Locate every blood parasite and identify its species.
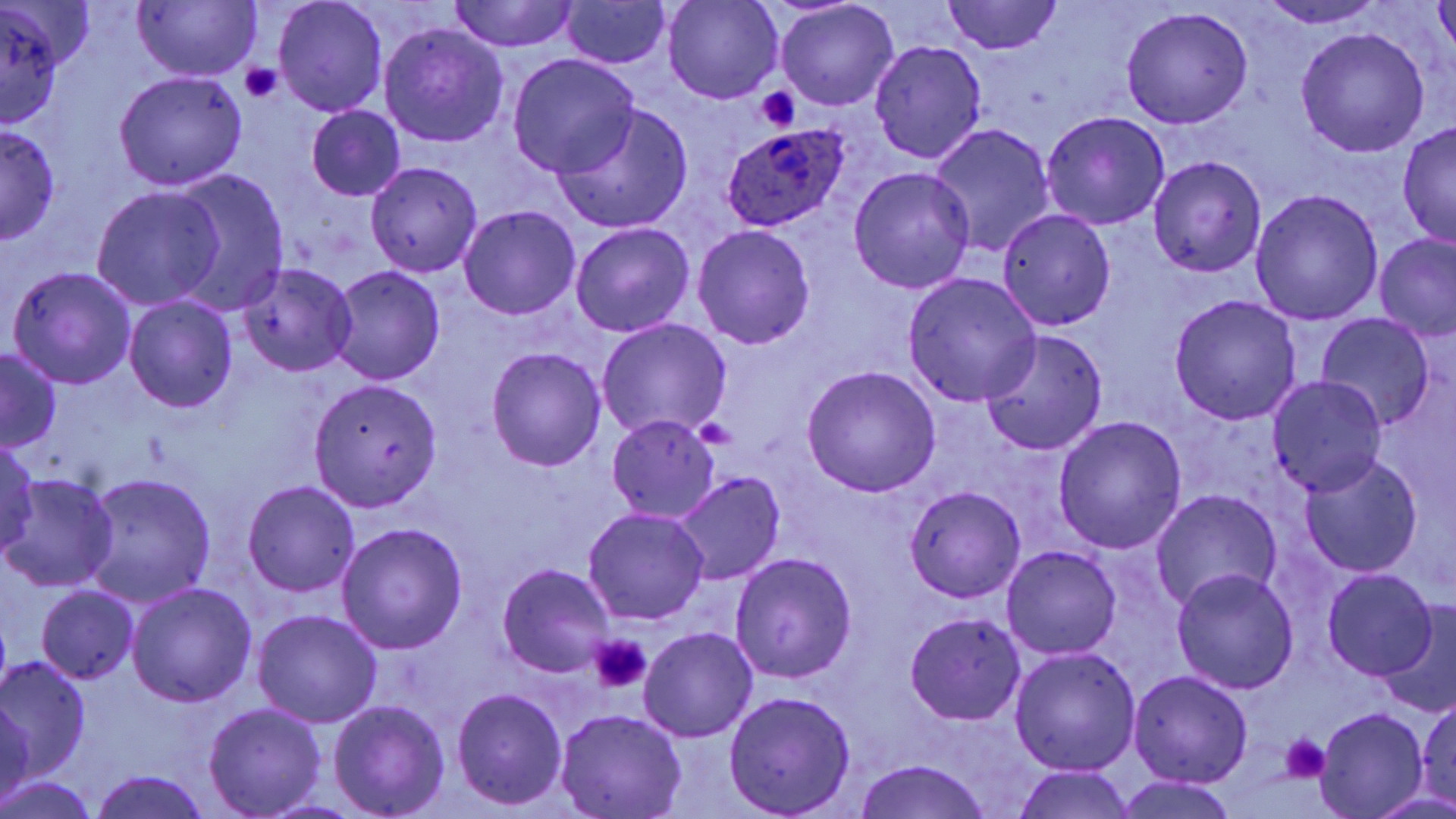

Approximate bounding boxes as (x1, y1, x2, y2) in pixels.
Plasmodium ovale-infected red blood cells: (720, 125, 847, 231).
No Plasmodium falciparum, Plasmodium malariae, Plasmodium vivax, Babesia divergens, or Trypanosoma brucei observed.

Uninfected red blood cell locations: (662, 0, 783, 104), (3, 1, 97, 73), (272, 1, 388, 116), (449, 1, 580, 53), (558, 1, 674, 70), (941, 1, 1064, 56), (1258, 1, 1389, 28), (775, 2, 900, 109), (1432, 2, 1456, 60), (1, 3, 66, 127), (131, 3, 260, 81), (1121, 7, 1254, 129), (380, 23, 508, 148), (1295, 27, 1429, 156), (869, 41, 988, 164), (508, 54, 639, 178), (114, 70, 247, 191), (553, 103, 693, 235), (306, 106, 405, 201), (1041, 111, 1171, 230), (1, 122, 60, 243), (928, 123, 1057, 256), (1397, 123, 1456, 248), (1148, 156, 1266, 278), (366, 161, 482, 277), (849, 167, 976, 293), (172, 170, 288, 308), (91, 187, 221, 310), (1250, 188, 1384, 326), (460, 205, 581, 318), (997, 209, 1116, 330), (570, 221, 696, 337), (692, 225, 816, 350), (1375, 235, 1456, 342), (238, 262, 359, 377), (8, 266, 137, 390), (330, 266, 445, 386), (903, 273, 1041, 407), (125, 295, 237, 414), (1170, 295, 1302, 426), (1315, 314, 1436, 432), (597, 318, 731, 442), (981, 328, 1107, 456), (486, 345, 607, 470), (1, 348, 63, 454), (802, 366, 941, 498), (1267, 376, 1389, 498), (308, 377, 443, 510), (606, 415, 719, 522), (1053, 416, 1187, 553), (1, 434, 42, 557), (1299, 454, 1423, 579), (669, 471, 786, 584), (3, 472, 119, 593), (82, 473, 216, 607), (242, 481, 360, 598), (904, 486, 1026, 603), (1151, 490, 1282, 615), (582, 506, 710, 626), (338, 523, 467, 653), (1002, 545, 1120, 659), (730, 553, 857, 682), (497, 563, 615, 677), (1172, 568, 1299, 695), (1322, 569, 1437, 682), (127, 583, 256, 705), (35, 586, 139, 682), (1379, 605, 1456, 715), (252, 610, 382, 727), (905, 613, 1026, 725), (639, 627, 758, 743), (1011, 646, 1141, 774), (0, 656, 93, 781), (1129, 670, 1253, 787), (451, 687, 567, 810), (725, 692, 856, 817), (1415, 694, 1456, 805), (0, 695, 38, 807), (330, 700, 449, 817), (203, 703, 326, 817), (555, 708, 688, 819), (1318, 708, 1428, 819), (851, 759, 994, 819), (1010, 766, 1138, 819), (90, 770, 212, 819), (0, 776, 101, 818), (1115, 776, 1241, 819), (1365, 789, 1456, 819). Platelet locations: (240, 62, 281, 104), (755, 86, 800, 130), (692, 415, 737, 450), (588, 633, 653, 694), (1280, 732, 1333, 782). Slide-level diagnosis: Plasmodium ovale. One field of a larger specimen. Image is 1456×819 pixels. Thin blood smear. Light microscopy. Captured at 1000x magnification. May-Grünwald-Giemsa stain.